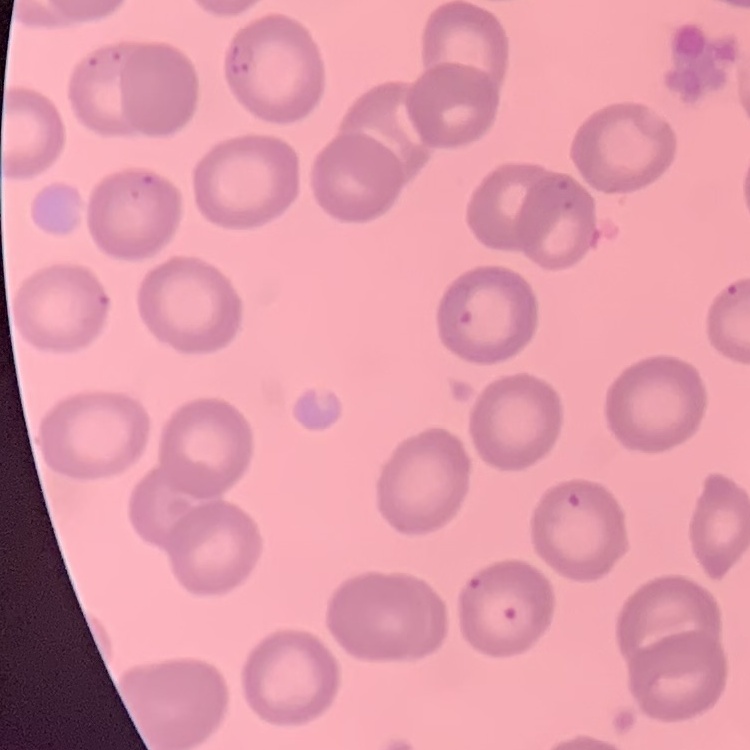
The erythrocytes show no rouleaux formation. Square crop of a larger photomicrograph. Thin blood smear. Field's or Giemsa stain.